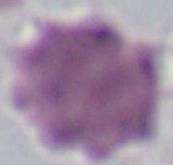

1000x magnification. Photomicrograph. A red blood cell is shown.